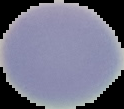
Summary:
  - Image size: 124×109 pixels
  - Preparation: thin blood smear
  - Malaria status: uninfected
  - Image type: cell region segmented out of the field of view; surrounding area masked to black